Comment on the morphology of the red blood cells.
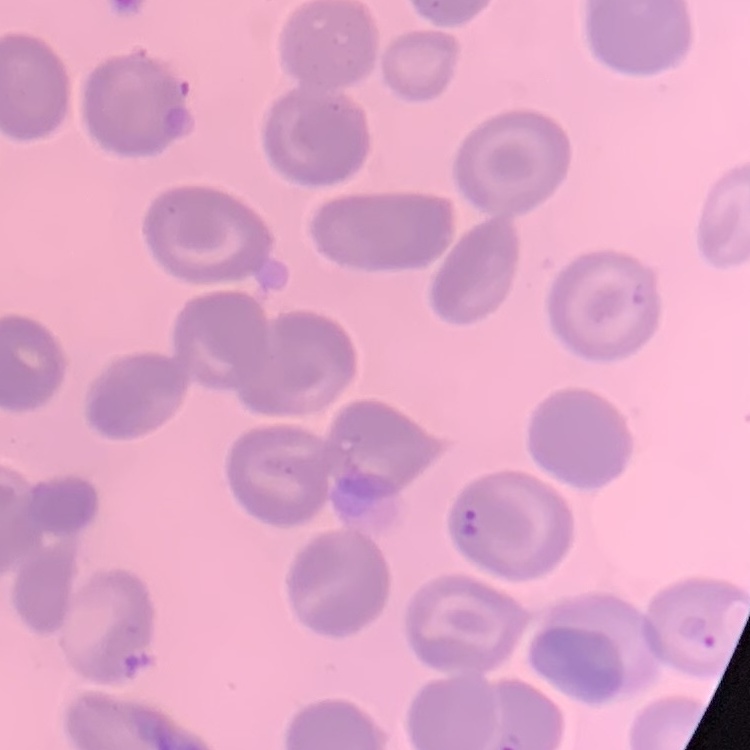
They show no rouleaux formation.

Summary:
  - Stain: Field's or Giemsa
  - Image type: square crop of a larger photomicrograph
  - Preparation: thin blood film